Describe the morphology of the red blood cells.
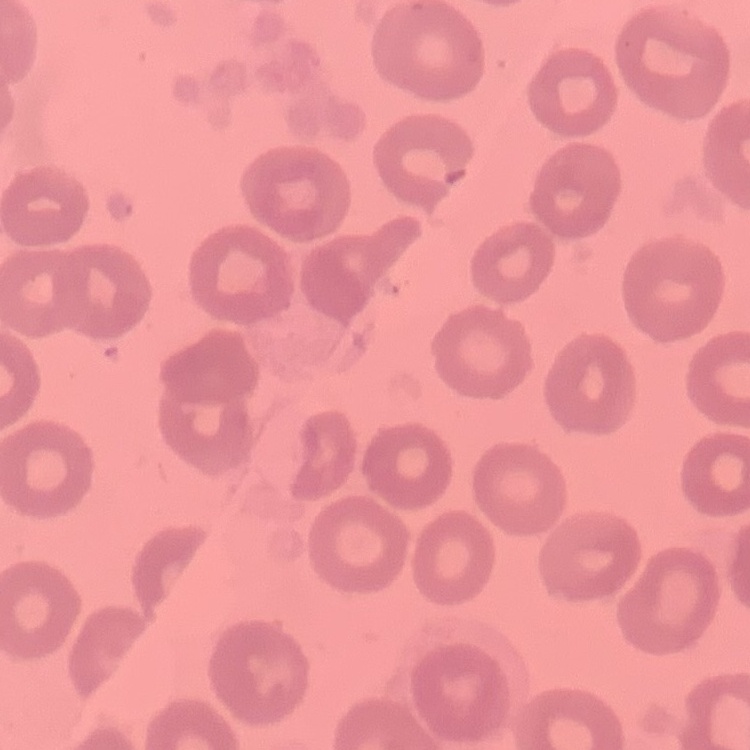
No rouleaux formation.

Square crop of a larger photomicrograph. Thin blood smear. Field's or Giemsa stain.